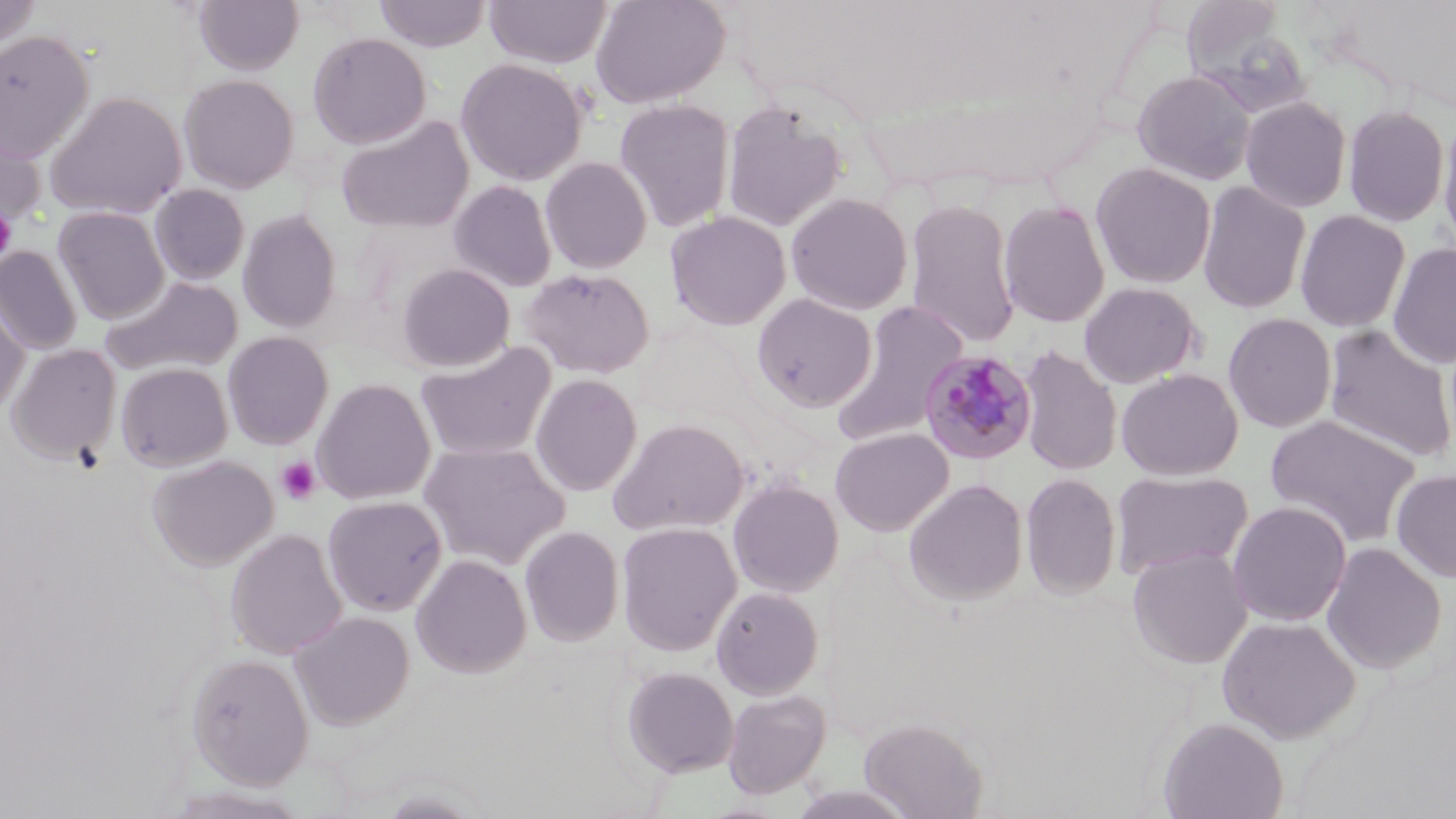
slide-level diagnosis = Plasmodium malariae
platelet locations = approximate bounding boxes as [x1, y1, x2, y2] in pixels: [0, 205, 17, 263], [275, 455, 322, 506]
modality = light microscopy
uninfected red blood cell locations = approximate bounding boxes as [x1, y1, x2, y2] in pixels: [0, 0, 43, 51], [193, 0, 304, 75], [373, 0, 492, 52], [484, 0, 613, 69], [590, 0, 730, 108], [1184, 7, 1316, 118], [0, 30, 95, 160], [307, 32, 431, 149], [455, 57, 588, 186], [1132, 69, 1257, 186], [179, 74, 300, 193], [45, 91, 187, 220], [1240, 97, 1352, 213], [614, 98, 735, 233], [722, 101, 847, 233], [1343, 105, 1449, 227], [1437, 113, 1456, 257], [336, 115, 474, 235], [0, 117, 45, 230], [540, 157, 652, 273], [1091, 162, 1216, 289], [449, 179, 558, 292], [1197, 181, 1311, 315], [150, 184, 250, 285], [786, 193, 913, 315], [998, 199, 1111, 328], [905, 200, 1021, 349], [53, 206, 170, 324], [1294, 209, 1410, 332], [237, 210, 342, 334], [666, 211, 791, 330], [1388, 241, 1456, 369], [0, 246, 83, 355], [396, 263, 515, 372], [520, 267, 655, 378], [100, 275, 244, 378], [1079, 281, 1202, 388], [0, 294, 29, 416], [752, 294, 877, 411], [831, 300, 969, 447], [1223, 313, 1337, 433], [1323, 324, 1456, 465], [222, 332, 333, 449], [415, 340, 557, 463], [7, 344, 122, 463], [1017, 345, 1123, 476], [116, 363, 233, 471], [1116, 368, 1243, 481], [530, 373, 643, 496], [313, 378, 436, 504], [1265, 414, 1422, 548], [607, 417, 750, 536], [830, 427, 954, 536], [419, 441, 570, 570], [147, 455, 278, 571], [1111, 469, 1252, 579], [1391, 469, 1456, 582], [1020, 472, 1121, 600], [727, 479, 844, 597], [904, 479, 1028, 605], [323, 496, 447, 616], [1227, 500, 1352, 627], [616, 522, 742, 657], [520, 525, 624, 646], [225, 528, 347, 660], [1321, 542, 1447, 675], [1127, 546, 1252, 669], [411, 554, 532, 678], [711, 586, 824, 699], [289, 611, 414, 730], [1216, 615, 1362, 744], [185, 652, 314, 788], [620, 666, 739, 778], [722, 689, 831, 799], [859, 716, 987, 819], [1157, 716, 1288, 819], [161, 786, 311, 819], [374, 789, 490, 819]
image size = 1456×819 pixels
Plasmodium malariae-infected red blood cell locations = approximate bounding boxes as [x1, y1, x2, y2] in pixels: [918, 348, 1039, 466]
preparation = thin blood film
field of view = one of a larger specimen
magnification = 1000x
stain = May-Grünwald-Giemsa